Give the position of every leukocyte visible.
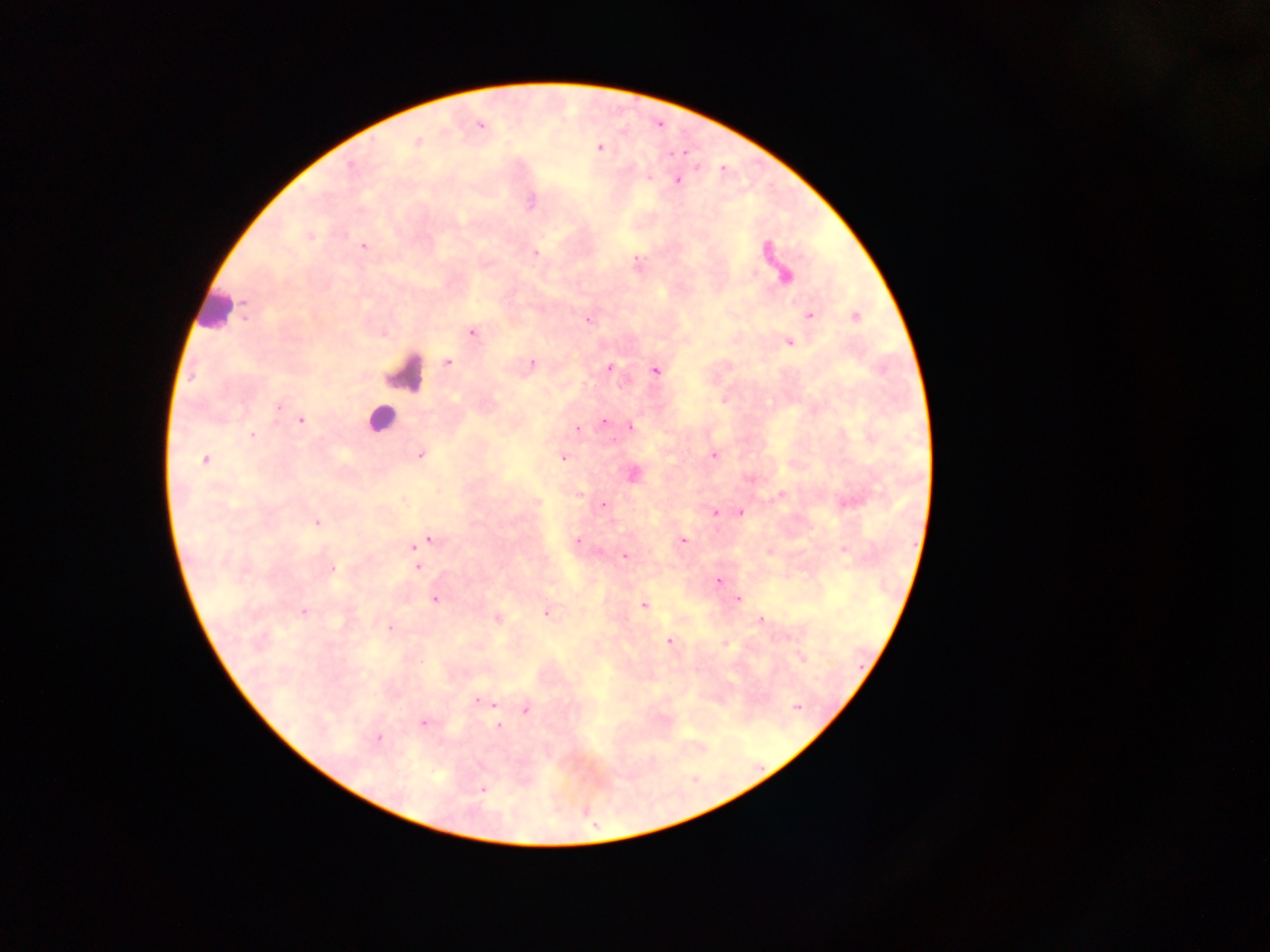
Approximate centers as [x, y] in pixels.
Leukocytes: [216, 310], [407, 374], [380, 419].

Summary:
  - Malaria parasite locations: [481, 126], [418, 142], [599, 147], [350, 166], [649, 178], [677, 181], [310, 237], [363, 246], [766, 250], [536, 253], [785, 277], [809, 315], [856, 317], [588, 319], [473, 333], [789, 342], [448, 362], [532, 364], [609, 367], [655, 372], [278, 405], [301, 421], [604, 422], [631, 427], [578, 429], [252, 435], [420, 455], [714, 455], [563, 458], [205, 460], [633, 474], [580, 494], [782, 494], [537, 502], [603, 505], [716, 513], [741, 513], [317, 523], [577, 539], [430, 540], [683, 541], [422, 543], [414, 547], [844, 550], [625, 556], [418, 567], [333, 569], [718, 581], [435, 600], [738, 600], [643, 604], [303, 612], [547, 613], [497, 618], [761, 620], [390, 627], [669, 642], [725, 643], [801, 658], [478, 701], [494, 705], [797, 707], [526, 711], [424, 722], [499, 727], [379, 738], [483, 788]
  - Field of view: single
  - Country: Ghana
  - Image size: 1270×952 pixels
  - Capture: mobile-phone photograph through a microscope
  - Preparation: thick blood smear